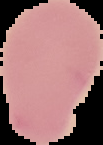 Result: negative for Plasmodium parasites. From a thin blood smear. Image is 103×145 pixels. The area outside the segmented cell region is set to black.